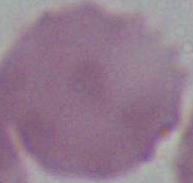
modality: micrograph
identification: erythrocyte
magnification: 1000x